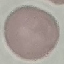

malaria status = uninfected
preparation = thin smear
stain = Giemsa
capture = smartphone through the microscope eyepiece
image type = cell patch, automatically extracted from a larger field of view and resized to 64 × 64 pixels